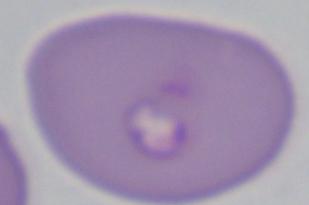

A Babesia parasite is shown. Photomicrograph. 1000x magnification.